Name the cell type shown.
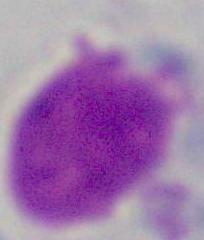
A leukocyte.

Summary:
  - Magnification: 1000x
  - Modality: micrograph